Identify the cell.
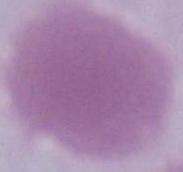
This is an erythrocyte.

Summary:
  - Magnification: 1000x
  - Modality: micrograph